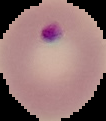
Summary:
  - Image size: 106×121 pixels
  - Preparation: thin blood smear
  - Result: Plasmodium parasites identified
  - Image type: cell region segmented out of the field of view; surrounding area masked to black